State which cell type is depicted.
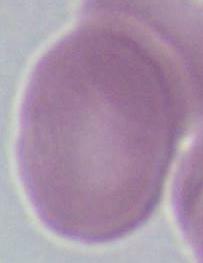
This is an erythrocyte.

Micrograph. Captured at 1000x magnification.